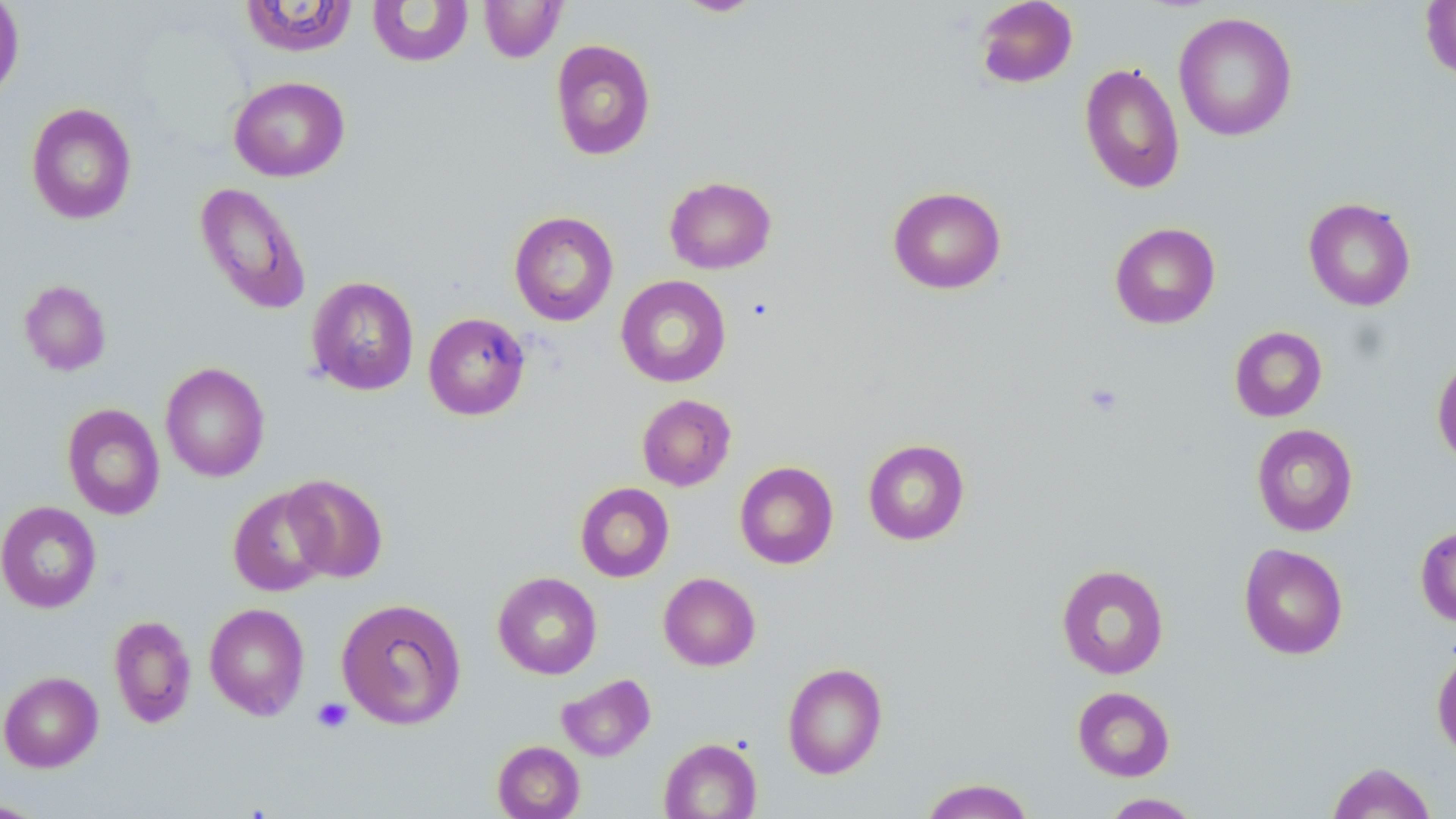
slide_level_diagnosis: negative for blood parasites
image_size: 1456×819 pixels
platelet_locations: 'approximate bounding boxes as [x1, y1, x2, y2] in pixels: [1084, 382, 1124, 417], [311, 697, 353, 734]'
modality: optical microscopy
stain: May-Grünwald-Giemsa
magnification: 1000x
uninfected_red_blood_cell_locations: 'approximate bounding boxes as [x1, y1, x2, y2] in pixels: [0, 0, 24, 102], [239, 0, 359, 57], [673, 0, 765, 17], [974, 0, 1078, 89], [1419, 0, 1456, 82], [367, 1, 474, 67], [479, 1, 566, 63], [1173, 12, 1297, 142], [550, 39, 656, 161], [1079, 62, 1185, 195], [229, 76, 349, 182], [25, 103, 138, 225], [664, 176, 777, 274], [195, 182, 311, 315], [887, 186, 1006, 294], [1303, 197, 1416, 311], [509, 211, 619, 326], [1109, 222, 1220, 329], [615, 275, 731, 388], [306, 276, 419, 396], [19, 279, 112, 376], [423, 312, 530, 420], [1229, 326, 1328, 422], [1432, 356, 1456, 467], [160, 362, 270, 481], [637, 394, 736, 491], [62, 403, 165, 520], [1251, 424, 1358, 536], [862, 439, 970, 545], [734, 461, 839, 569], [282, 474, 388, 583], [574, 482, 674, 582], [228, 486, 333, 596], [0, 501, 101, 613], [1415, 525, 1456, 628], [1238, 543, 1348, 660], [1056, 563, 1169, 679], [492, 571, 602, 679], [658, 572, 761, 670], [336, 597, 466, 730], [204, 603, 309, 720], [108, 615, 196, 728], [1432, 646, 1456, 761], [782, 662, 887, 779], [0, 670, 103, 772], [557, 673, 656, 762], [1072, 686, 1175, 781], [658, 737, 762, 818], [492, 741, 585, 819], [1325, 761, 1437, 819], [919, 778, 1036, 819], [1099, 793, 1203, 818], [0, 797, 50, 818]'
preparation: thin blood smear
field_of_view: single